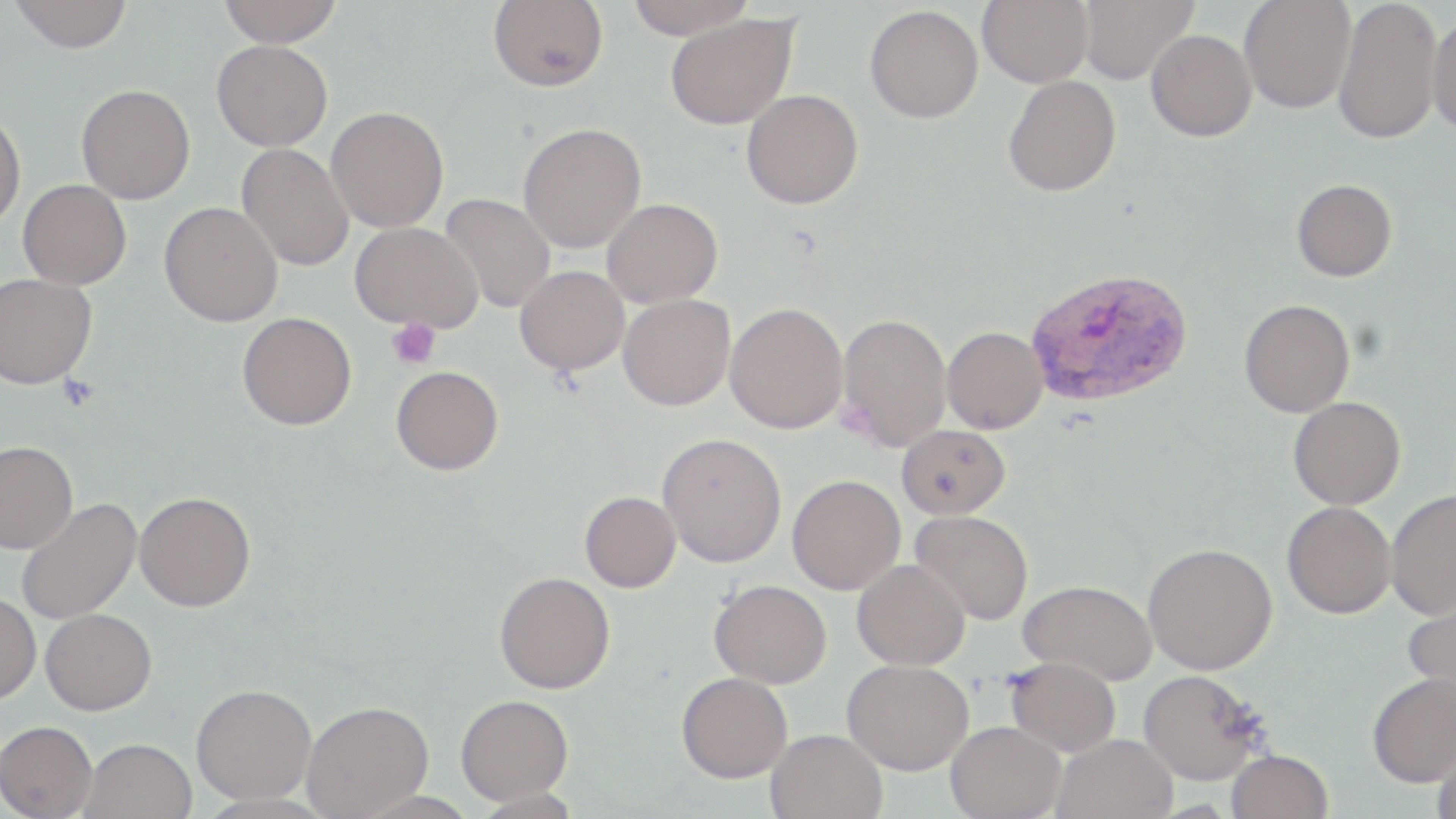
Summary:
  - Coordinate format: approximate bounding boxes as [x1, y1, x2, y2] in pixels
  - Plasmodium vivax-infected red blood cell locations: [1025, 266, 1193, 407]
  - Uninfected red blood cell locations: [7, 0, 134, 53], [215, 0, 345, 45], [624, 0, 757, 39], [978, 0, 1092, 87], [1077, 0, 1197, 83], [1239, 0, 1355, 113], [1333, 0, 1443, 144], [488, 1, 608, 92], [865, 5, 983, 123], [664, 13, 798, 129], [1426, 13, 1456, 139], [1145, 29, 1257, 141], [211, 40, 332, 151], [1003, 75, 1121, 197], [76, 84, 195, 204], [741, 89, 863, 209], [326, 106, 449, 232], [0, 110, 26, 233], [518, 122, 646, 253], [236, 143, 354, 271], [1292, 179, 1397, 282], [18, 180, 132, 289], [439, 193, 556, 313], [602, 198, 722, 308], [159, 201, 283, 327], [350, 221, 482, 332], [515, 265, 630, 376], [0, 273, 97, 389], [618, 294, 735, 411], [1239, 299, 1355, 417], [724, 302, 849, 433], [237, 312, 357, 430], [837, 313, 951, 451], [942, 326, 1048, 434], [391, 365, 503, 475], [1288, 397, 1405, 509], [896, 424, 1010, 520], [657, 432, 786, 568], [0, 440, 78, 553], [787, 474, 905, 594], [1385, 490, 1456, 620], [134, 491, 255, 611], [579, 491, 681, 592], [16, 497, 141, 624], [1282, 501, 1395, 618], [910, 509, 1033, 625], [1143, 542, 1277, 674], [852, 559, 970, 670], [494, 571, 615, 694], [708, 579, 833, 688], [1018, 579, 1157, 685], [1401, 587, 1456, 702], [0, 592, 41, 704], [41, 608, 156, 715], [1005, 656, 1121, 757], [842, 658, 974, 774], [1138, 669, 1270, 786], [1366, 671, 1456, 787], [676, 672, 792, 782], [191, 683, 316, 804], [455, 694, 573, 805], [301, 700, 434, 817], [0, 720, 98, 818], [946, 720, 1066, 819], [765, 728, 888, 819], [1051, 733, 1179, 819], [1432, 737, 1456, 815], [78, 738, 198, 819], [1226, 749, 1332, 819]
  - Platelet locations: [386, 318, 440, 370]
  - Slide-level diagnosis: Plasmodium vivax
  - Magnification: 1000x
  - Preparation: thin blood smear
  - Field of view: single
  - Stain: May-Grünwald-Giemsa
  - Modality: light microscopy
  - Image size: 1456×819 pixels